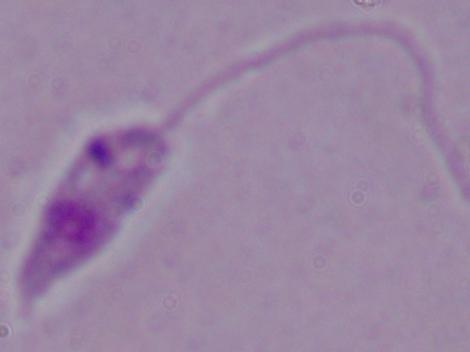 Captured at 1000x magnification. A Leishmania parasite is seen. Photomicrograph.